Identify the parasite.
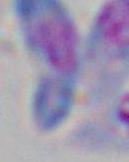

This is Toxoplasma gondii.

modality = photomicrograph
magnification = 1000x